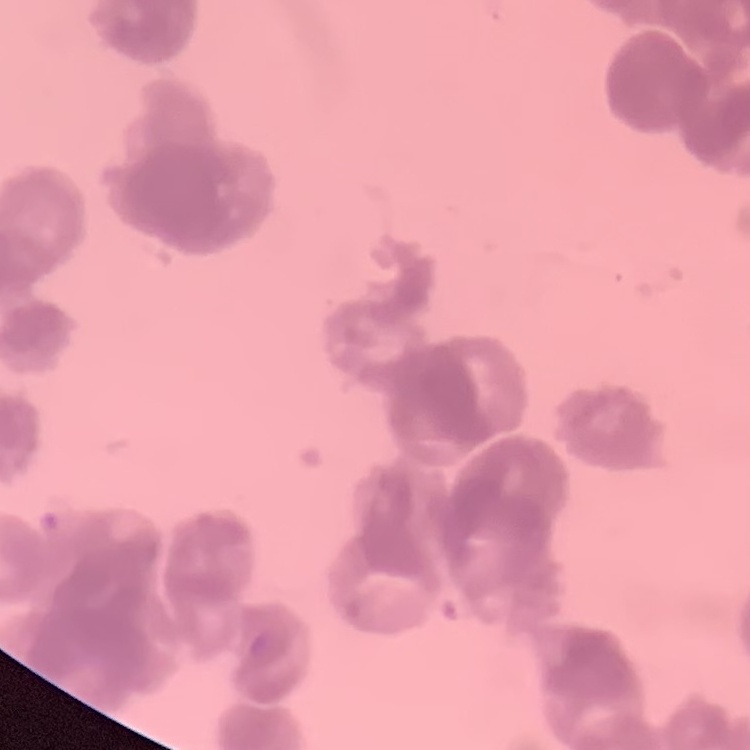
Summary:
  - Red blood cell morphology: rouleaux formation
  - Stain: Field's or Giemsa
  - Image type: one tile cut from a larger photomicrograph
  - Preparation: thin peripheral smear